Point out each malaria parasite and each leukocyte.
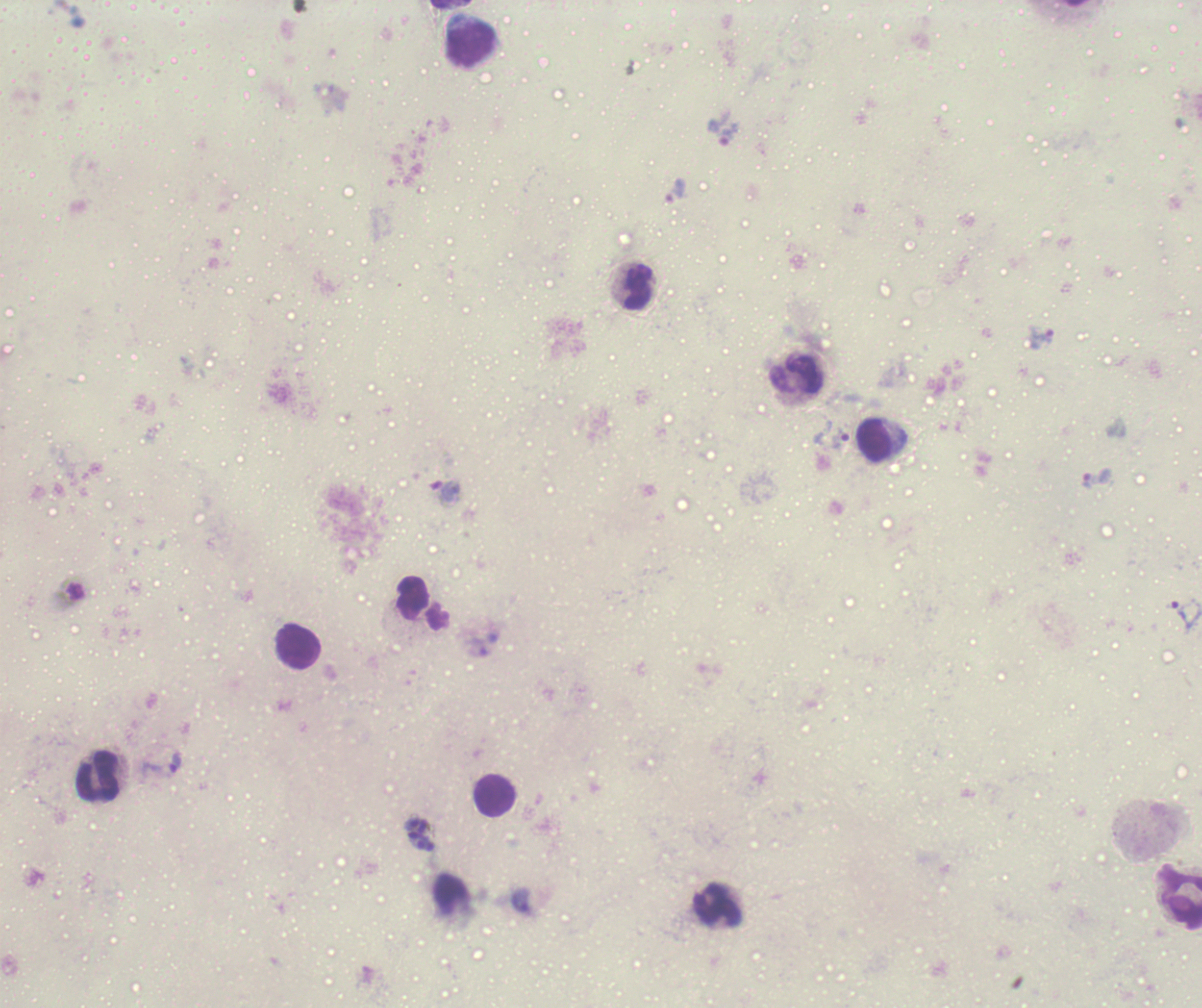

Approximate centers as [x, y] in pixels.
Trophozoites: [722, 132], [676, 191], [1041, 339], [840, 439], [1097, 479], [445, 492], [1185, 614], [162, 763].
Schizonts: [419, 835].
No gametocyte forms observed.
Leukocytes: [470, 43], [639, 287], [797, 375], [875, 441], [299, 648], [98, 776], [495, 795], [1180, 898], [718, 905].

{
  "field_of_view": "single",
  "background_quality": "poor",
  "preparation": "thick blood smear",
  "coloration_quality": "bad",
  "context": "previously used in a real diagnosis",
  "magnification": "100x",
  "image_size": "1202×1008 pixels",
  "stain": "Romanowsky"
}